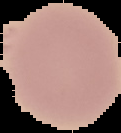

image type = cell region segmented out of the field of view; surrounding area masked to black
preparation = thin blood film
image size = 121×133 pixels
result = negative for malaria parasites